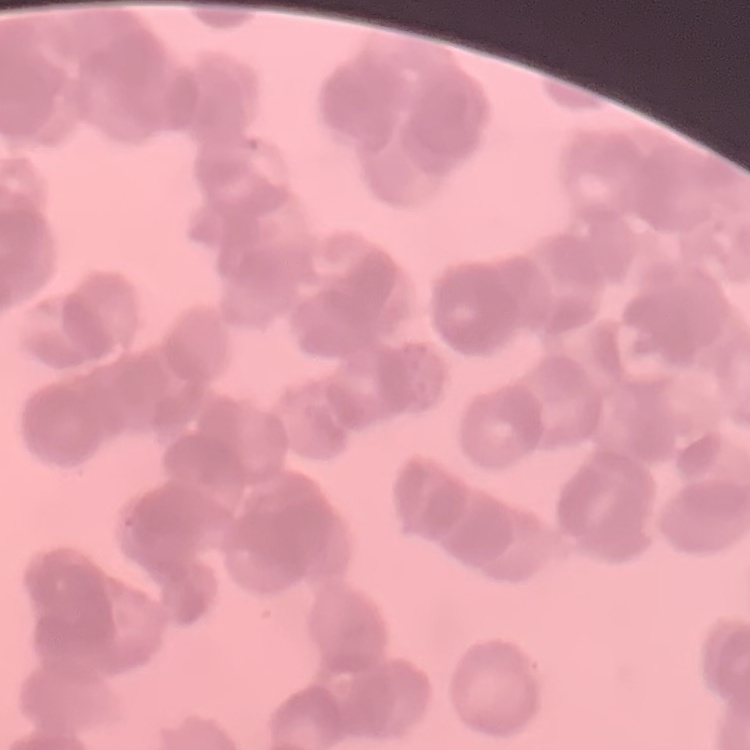
The red blood cells exhibit rouleaux formation. Square crop of a larger photomicrograph. Thin blood film. Field's or Giemsa stain.